Assess this cell for malaria.
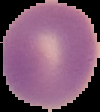

Uninfected.

From a thin blood smear. Cell region segmented out of the field of view; the surrounding area is masked to black. Image is 100×112 pixels.